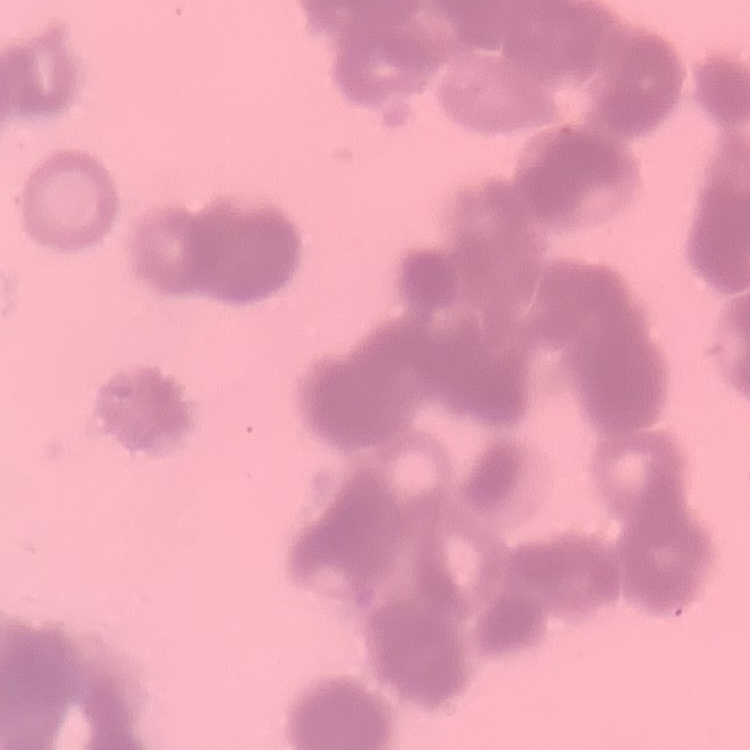

{
  "red_blood_cell_morphology": "rouleaux formation",
  "image_type": "one tile cut from a larger photomicrograph",
  "stain": "Field's or Giemsa",
  "preparation": "thin peripheral smear"
}